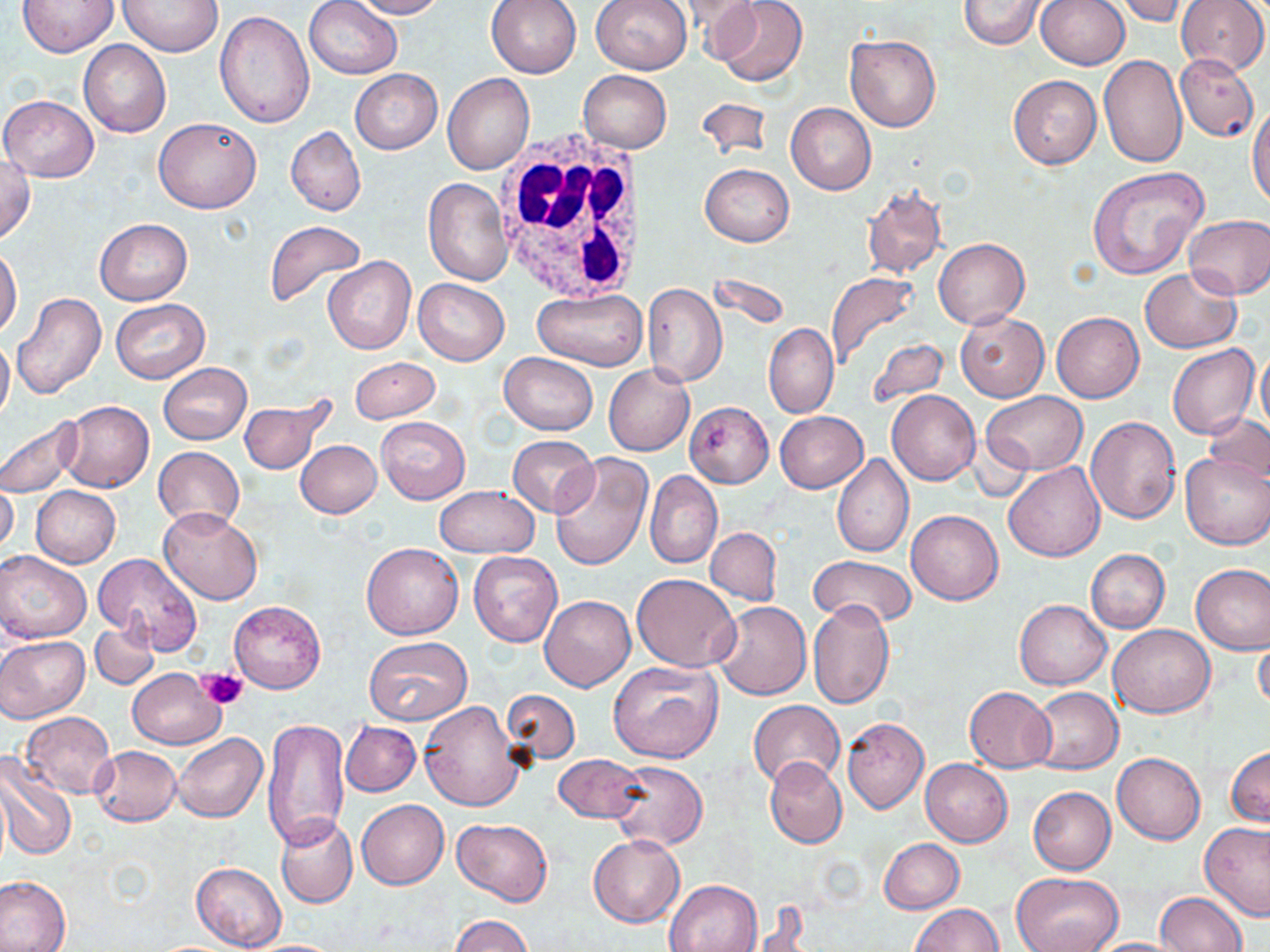

slide_level_diagnosis: no evidence of blood parasites
modality: light microscopy
uninfected_red_blood_cell_locations: 'approximate bounding boxes as [x1, y1, x2, y2] in pixels: [19, 0, 118, 55], [305, 0, 402, 79], [350, 0, 447, 18], [485, 0, 582, 78], [675, 0, 764, 49], [710, 0, 809, 87], [958, 0, 1048, 51], [1115, 0, 1190, 26], [1176, 0, 1269, 75], [120, 1, 223, 56], [591, 1, 692, 75], [1037, 1, 1129, 71], [214, 12, 312, 129], [845, 34, 941, 132], [78, 41, 171, 137], [1098, 54, 1188, 168], [1175, 54, 1259, 142], [350, 69, 442, 154], [579, 70, 671, 152], [441, 74, 533, 174], [1008, 74, 1101, 168], [1, 95, 98, 182], [694, 97, 774, 161], [1248, 102, 1270, 210], [786, 103, 876, 194], [154, 116, 261, 213], [286, 126, 366, 217], [0, 155, 35, 244], [700, 164, 794, 247], [1087, 167, 1209, 279], [423, 178, 512, 285], [861, 184, 947, 279], [1184, 213, 1270, 300], [95, 218, 192, 305], [262, 219, 367, 311], [933, 238, 1028, 328], [0, 247, 21, 339], [323, 256, 416, 355], [1140, 268, 1243, 353], [709, 272, 790, 331], [826, 272, 920, 367], [414, 278, 509, 365], [642, 283, 727, 387], [533, 289, 647, 370], [11, 292, 106, 399], [111, 300, 209, 383], [955, 311, 1050, 402], [1052, 312, 1144, 403], [763, 323, 838, 417], [0, 334, 14, 425], [866, 338, 949, 412], [1167, 344, 1259, 439], [1256, 344, 1270, 438], [498, 353, 597, 434], [349, 357, 440, 421], [158, 362, 252, 444], [603, 366, 694, 455], [887, 390, 979, 485], [982, 392, 1088, 474], [239, 396, 337, 476], [59, 401, 154, 492], [683, 401, 774, 488], [775, 411, 868, 493], [1203, 413, 1269, 486], [0, 416, 83, 498], [376, 416, 470, 505], [1086, 416, 1181, 523], [507, 435, 598, 517], [295, 439, 382, 518], [153, 447, 244, 531], [547, 452, 653, 573], [1180, 453, 1270, 551], [832, 454, 913, 558], [1004, 463, 1104, 562], [645, 470, 722, 570], [0, 478, 19, 560], [30, 486, 120, 568], [433, 486, 540, 557], [157, 508, 264, 605], [906, 510, 1003, 605], [705, 527, 781, 605], [361, 542, 463, 639], [0, 550, 91, 642], [1087, 550, 1169, 633], [468, 551, 563, 646], [94, 553, 204, 654], [809, 555, 917, 628], [1191, 563, 1270, 654], [632, 574, 741, 672], [539, 595, 636, 691], [1014, 599, 1111, 690], [229, 600, 326, 694], [807, 600, 896, 710], [713, 601, 811, 701], [90, 620, 161, 689], [1109, 623, 1215, 717], [0, 635, 89, 723], [365, 636, 473, 724], [1253, 637, 1270, 715], [607, 659, 724, 764], [129, 668, 225, 748], [964, 687, 1056, 772], [1026, 687, 1123, 774], [504, 690, 578, 765], [749, 700, 844, 787], [419, 701, 523, 812], [20, 711, 117, 798], [261, 717, 351, 850], [842, 718, 929, 813], [340, 720, 420, 797], [173, 733, 267, 822], [91, 746, 181, 825], [1227, 746, 1269, 827], [1112, 752, 1205, 844], [554, 755, 648, 825], [0, 756, 75, 861], [764, 758, 846, 848], [920, 759, 1012, 846], [610, 761, 708, 851], [1028, 786, 1117, 874], [357, 799, 448, 890], [275, 815, 358, 907], [452, 818, 554, 906], [1201, 822, 1270, 920], [588, 835, 684, 927], [879, 838, 964, 914], [191, 862, 286, 950], [1010, 871, 1124, 952], [0, 876, 71, 952], [664, 879, 763, 952], [1155, 892, 1247, 952], [744, 904, 811, 952], [912, 904, 1005, 951], [450, 914, 533, 952], [1083, 937, 1191, 951]'
stain: May-Grünwald-Giemsa
magnification: 1000x
image_size: 1270×952 pixels
field_of_view: one of a larger specimen
platelet_locations: 'approximate bounding boxes as [x1, y1, x2, y2] in pixels: [198, 669, 246, 709]'
preparation: thin blood smear
white_blood_cell_locations: 'approximate bounding boxes as [x1, y1, x2, y2] in pixels: [493, 132, 647, 301]'